Classify this cell by malaria status.
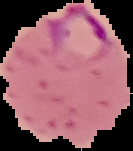
Parasitized.

Summary:
  - Image type: segmented cell region with the area outside set to black
  - Preparation: thin blood smear
  - Image size: 133×151 pixels